Comment on the morphology of the erythrocytes.
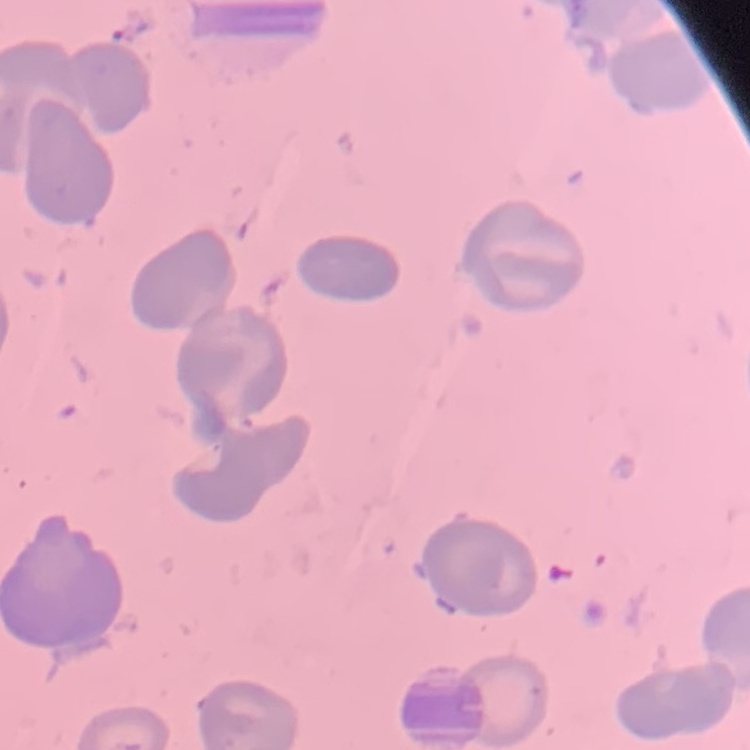
No rouleaux formation.

Summary:
  - Preparation: thin blood film
  - Image type: one tile cut from a larger photomicrograph
  - Stain: Field's or Giemsa